Identify the parasite.
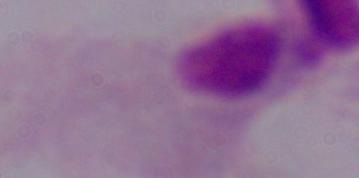

A trichomonad.

Micrograph. 1000x magnification.